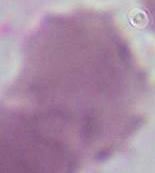
Summary:
  - Identification: red blood cell
  - Modality: photomicrograph
  - Magnification: 1000x